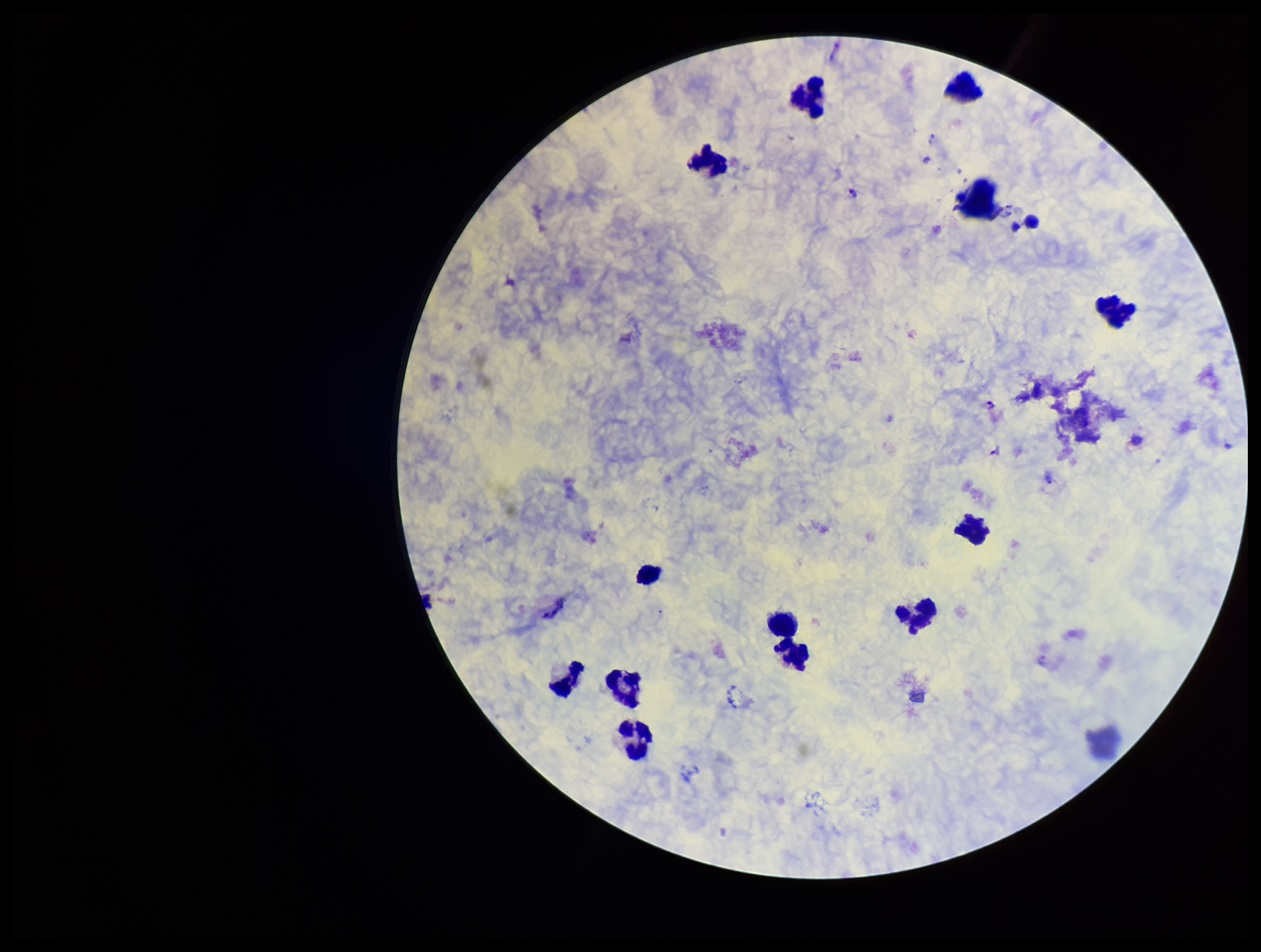
patient_malaria_status: infected
leukocyte_count: 13
field_of_view: one from this slide
preparation: thick smear
plasmodium_parasites: seen
image_size: 1261×952 pixels
parasite_count: 4
species_reported_for_this_patient: Plasmodium vivax
stain: Giemsa
capture: smartphone photograph through the microscope eyepiece